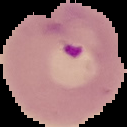

Summary:
  - Image size: 127×127 pixels
  - Image type: cell region segmented out of the field of view; surrounding area masked to black
  - Malaria status: parasitized
  - Preparation: thin blood smear